State which parasite is depicted.
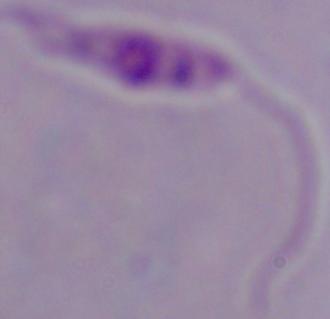
This is Leishmania.

modality = photomicrograph
magnification = 1000x